State the blood parasite species.
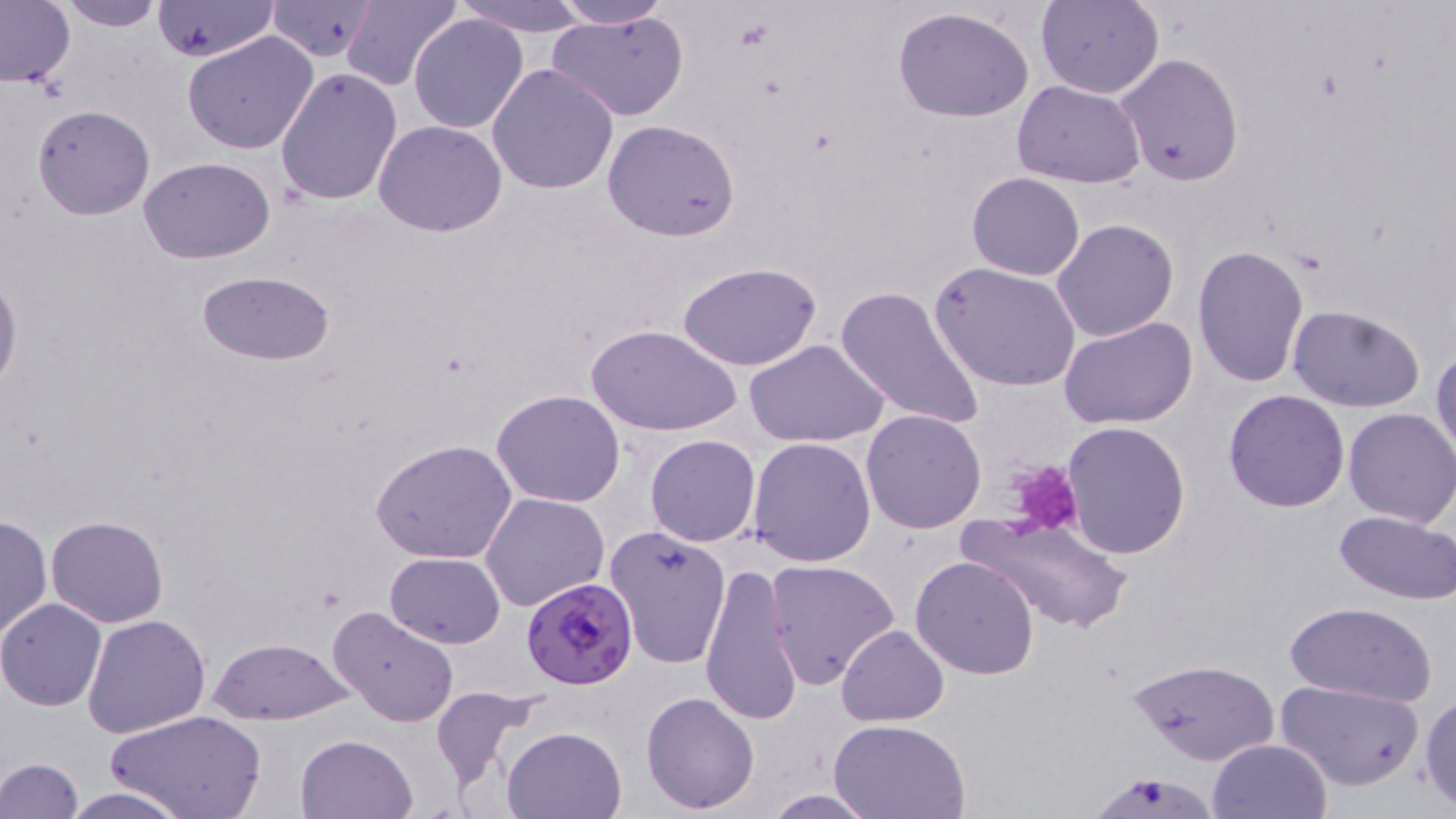

Plasmodium falciparum.

uninfected red blood cell locations = approximate bounding boxes as [x1, y1, x2, y2] in pixels: [153, 0, 279, 62], [455, 0, 591, 37], [550, 0, 674, 28], [1037, 0, 1164, 99], [0, 1, 76, 89], [57, 1, 168, 31], [267, 1, 378, 61], [336, 2, 461, 89], [893, 6, 1035, 123], [546, 9, 690, 123], [408, 12, 528, 134], [182, 32, 319, 155], [1115, 53, 1244, 185], [487, 63, 621, 194], [275, 66, 403, 206], [1012, 80, 1146, 186], [33, 104, 154, 220], [375, 119, 508, 237], [602, 119, 740, 241], [138, 156, 275, 263], [967, 172, 1085, 280], [1052, 218, 1178, 341], [1194, 244, 1308, 386], [678, 261, 822, 370], [930, 261, 1082, 392], [196, 270, 336, 364], [0, 271, 22, 395], [835, 284, 986, 431], [1286, 304, 1427, 414], [1060, 315, 1198, 429], [590, 323, 740, 436], [744, 339, 889, 448], [1431, 345, 1456, 464], [491, 389, 626, 509], [1224, 389, 1350, 513], [1342, 408, 1456, 527], [862, 409, 985, 534], [1061, 421, 1189, 560], [645, 433, 761, 546], [749, 438, 877, 568], [372, 439, 518, 564], [479, 492, 609, 612], [1334, 510, 1456, 603], [959, 512, 1132, 634], [0, 515, 51, 641], [45, 515, 169, 626], [605, 524, 731, 668], [385, 551, 506, 648], [910, 555, 1040, 679], [765, 559, 899, 689], [699, 560, 803, 728], [0, 598, 108, 710], [1282, 599, 1438, 705], [328, 605, 460, 731], [81, 612, 210, 739], [836, 624, 949, 727], [209, 636, 351, 725], [1130, 659, 1281, 772], [1276, 677, 1426, 791], [430, 685, 552, 795], [641, 691, 759, 811], [1420, 693, 1456, 811], [110, 710, 264, 819], [831, 717, 972, 818], [502, 726, 626, 819], [296, 735, 419, 819], [1207, 738, 1333, 819], [0, 757, 84, 818], [1086, 767, 1221, 819], [57, 787, 197, 819], [759, 789, 881, 818]
modality = optical microscopy
stain = May-Grünwald-Giemsa
magnification = 1000x
Plasmodium falciparum-infected red blood cell locations = approximate bounding boxes as [x1, y1, x2, y2] in pixels: [519, 579, 637, 694]
field of view = single
image size = 1456×819 pixels
platelet locations = approximate bounding boxes as [x1, y1, x2, y2] in pixels: [1009, 459, 1085, 537]
preparation = thin blood smear